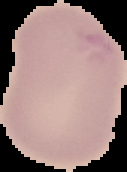
Result: negative for malaria parasites. Cell region segmented out of the field of view; the surrounding area is masked to black. Image is 127×172 pixels. From a thin blood film.